Comment on the morphology of the erythrocytes.
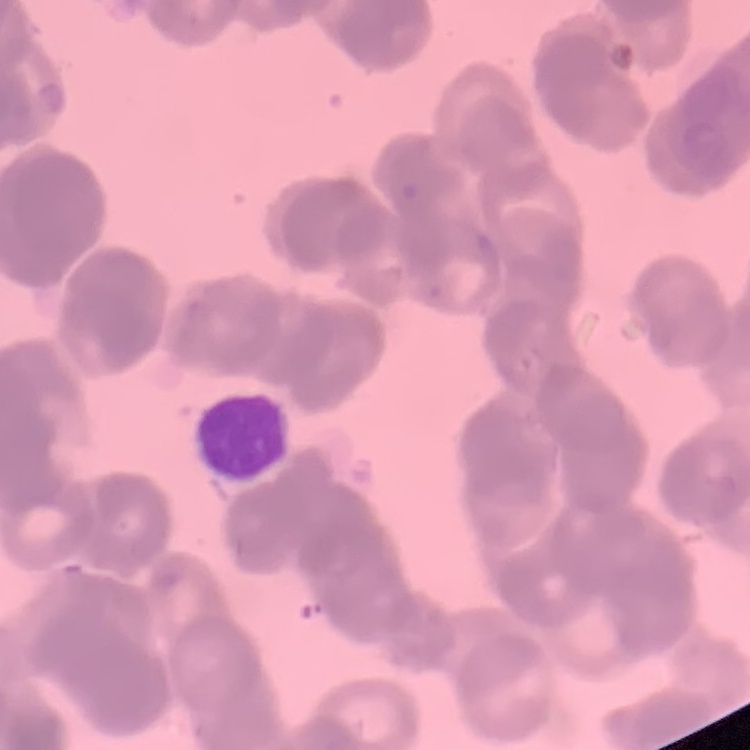

They show rouleaux formation.

Stained with either Field's or Giemsa. Square crop of a larger photomicrograph. Thin blood smear.